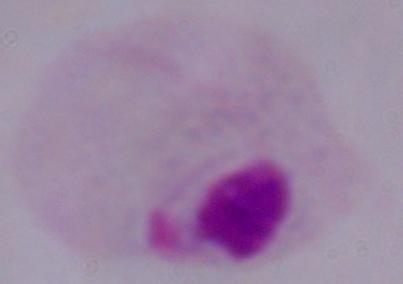

modality = photomicrograph
magnification = 1000x
identification = trichomonad